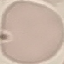
{
  "result": "no malaria parasites detected",
  "preparation": "thin blood film",
  "stain": "Giemsa",
  "capture": "smartphone camera at the microscope eyepiece",
  "image_type": "cell patch, automatically extracted from a larger field of view and resized to 64 × 64 pixels"
}